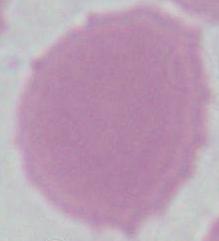
Summary:
  - Identification: red blood cell
  - Modality: micrograph
  - Magnification: 1000x